Find the red blood cells that are infected with P. falciparum, and any of indeterminate infection status.
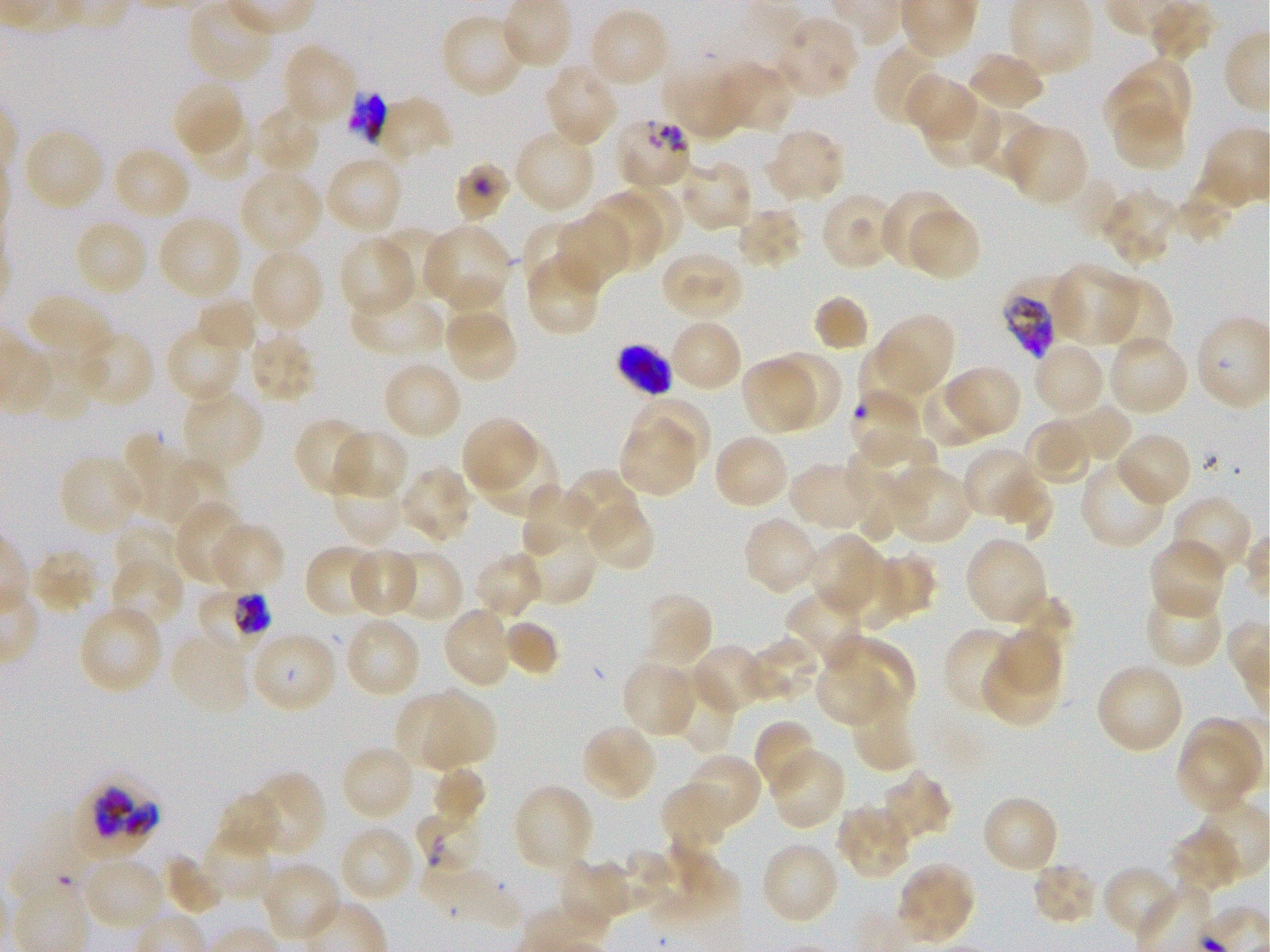

Approximate bounding boxes as (x1, y1, x2, y2) in pixels. Not every red blood cell is marked. A life-cycle stage — or a range of stages, where the recorded stages span more than one — follows each staged infected red blood cell.
Infected red blood cells: (199, 589, 271, 647) early trophozoite to early schizont; (88, 780, 157, 845).
Red blood cells of indeterminate infection status: (344, 90, 389, 146), (614, 115, 694, 190), (455, 163, 511, 223), (1003, 289, 1055, 359), (617, 345, 672, 397), (851, 389, 927, 465), (414, 804, 479, 867), (18, 825, 90, 896).

Locations of uninfected red blood cells: (586, 7, 670, 89), (440, 13, 529, 99), (771, 14, 858, 99), (874, 41, 949, 127), (281, 42, 358, 128), (966, 50, 1046, 113), (666, 58, 750, 141), (1118, 59, 1190, 136), (713, 61, 794, 135), (542, 62, 620, 148), (903, 74, 981, 144), (171, 77, 240, 150), (1105, 80, 1172, 137), (921, 94, 999, 169), (372, 97, 452, 164), (249, 104, 322, 177), (967, 106, 1045, 182), (1114, 107, 1187, 171), (196, 117, 253, 178), (1002, 122, 1089, 207), (765, 126, 846, 203), (21, 127, 105, 213), (513, 128, 597, 215), (111, 145, 192, 221), (323, 153, 404, 236), (676, 158, 755, 233), (238, 168, 324, 254), (623, 183, 680, 251), (1100, 188, 1179, 265), (819, 190, 901, 270), (880, 190, 959, 269), (586, 195, 662, 271), (905, 206, 981, 281), (735, 207, 805, 270), (156, 213, 244, 302), (552, 213, 634, 291), (73, 218, 149, 298), (523, 220, 590, 284), (420, 223, 512, 312), (378, 225, 452, 301), (337, 235, 416, 317), (248, 247, 325, 336), (659, 249, 746, 321), (523, 251, 603, 336), (1050, 263, 1139, 346), (444, 272, 510, 347), (1094, 277, 1172, 356), (349, 286, 446, 358), (27, 293, 115, 370), (813, 296, 868, 351), (195, 297, 259, 354), (871, 313, 955, 400), (450, 316, 517, 383), (668, 318, 744, 395), (165, 323, 246, 404), (248, 329, 317, 405), (74, 331, 155, 406), (1108, 333, 1190, 416), (859, 340, 930, 417), (1032, 341, 1106, 419), (24, 349, 92, 420), (778, 349, 842, 429), (740, 356, 818, 436), (381, 359, 463, 442), (942, 364, 1023, 438), (919, 379, 995, 447), (180, 387, 265, 474), (631, 396, 711, 467), (1039, 403, 1132, 470), (461, 416, 539, 497), (620, 417, 695, 495), (1026, 417, 1094, 484), (293, 418, 373, 497), (331, 428, 409, 500), (1114, 430, 1192, 507), (857, 431, 936, 505), (119, 432, 198, 524), (711, 433, 791, 510), (476, 438, 562, 520), (962, 446, 1035, 515), (58, 454, 144, 537), (844, 454, 905, 544), (1079, 457, 1169, 549), (329, 459, 408, 547), (162, 460, 229, 530), (789, 460, 878, 533), (886, 463, 973, 546), (398, 466, 475, 547), (564, 470, 646, 558), (991, 473, 1052, 540), (520, 484, 593, 561), (1171, 495, 1253, 579), (172, 499, 247, 585), (585, 501, 655, 572), (742, 516, 821, 596), (112, 521, 182, 591), (209, 523, 286, 595), (518, 527, 597, 606), (806, 534, 886, 620), (964, 535, 1050, 627), (1148, 538, 1227, 621), (304, 544, 384, 619), (30, 547, 100, 615), (386, 547, 465, 623), (346, 548, 419, 617), (472, 552, 544, 620), (876, 552, 943, 620), (110, 556, 187, 630), (831, 557, 902, 629), (1144, 584, 1223, 670), (784, 588, 868, 669), (643, 592, 714, 670), (76, 605, 164, 696), (440, 606, 514, 690), (342, 616, 422, 699), (503, 619, 558, 676), (942, 626, 1023, 716), (996, 628, 1062, 693), (169, 630, 252, 718), (248, 630, 338, 715), (740, 636, 823, 704), (829, 636, 915, 713), (689, 643, 771, 714), (620, 660, 700, 739), (979, 661, 1054, 727), (813, 662, 889, 727), (1095, 662, 1184, 756), (681, 685, 736, 754), (393, 688, 464, 771), (424, 692, 494, 767), (854, 697, 917, 773), (1186, 715, 1264, 791), (752, 719, 819, 795), (579, 723, 659, 803), (1175, 740, 1252, 814), (340, 744, 417, 822), (768, 747, 845, 831), (679, 753, 762, 834), (430, 766, 486, 827), (879, 770, 952, 847), (243, 772, 324, 858), (660, 782, 732, 843), (513, 783, 595, 875), (218, 791, 282, 858), (980, 794, 1060, 874), (836, 803, 914, 881), (338, 825, 419, 904), (201, 826, 279, 902), (1172, 826, 1244, 896), (659, 841, 741, 930), (759, 841, 840, 926), (598, 847, 669, 914), (161, 854, 225, 915), (80, 856, 168, 932), (556, 858, 617, 927), (415, 860, 518, 928), (259, 861, 342, 943), (894, 861, 976, 946), (1031, 861, 1099, 925), (1099, 865, 1180, 941). Giemsa stain. Thin blood film. Donor blood group O+. Single field of view. P. falciparum strain 3D7 in static in-vitro culture. Oil immersion, 100x objective (numerical aperture 1.25). Image is 1270×952 pixels.